Assess for malaria.
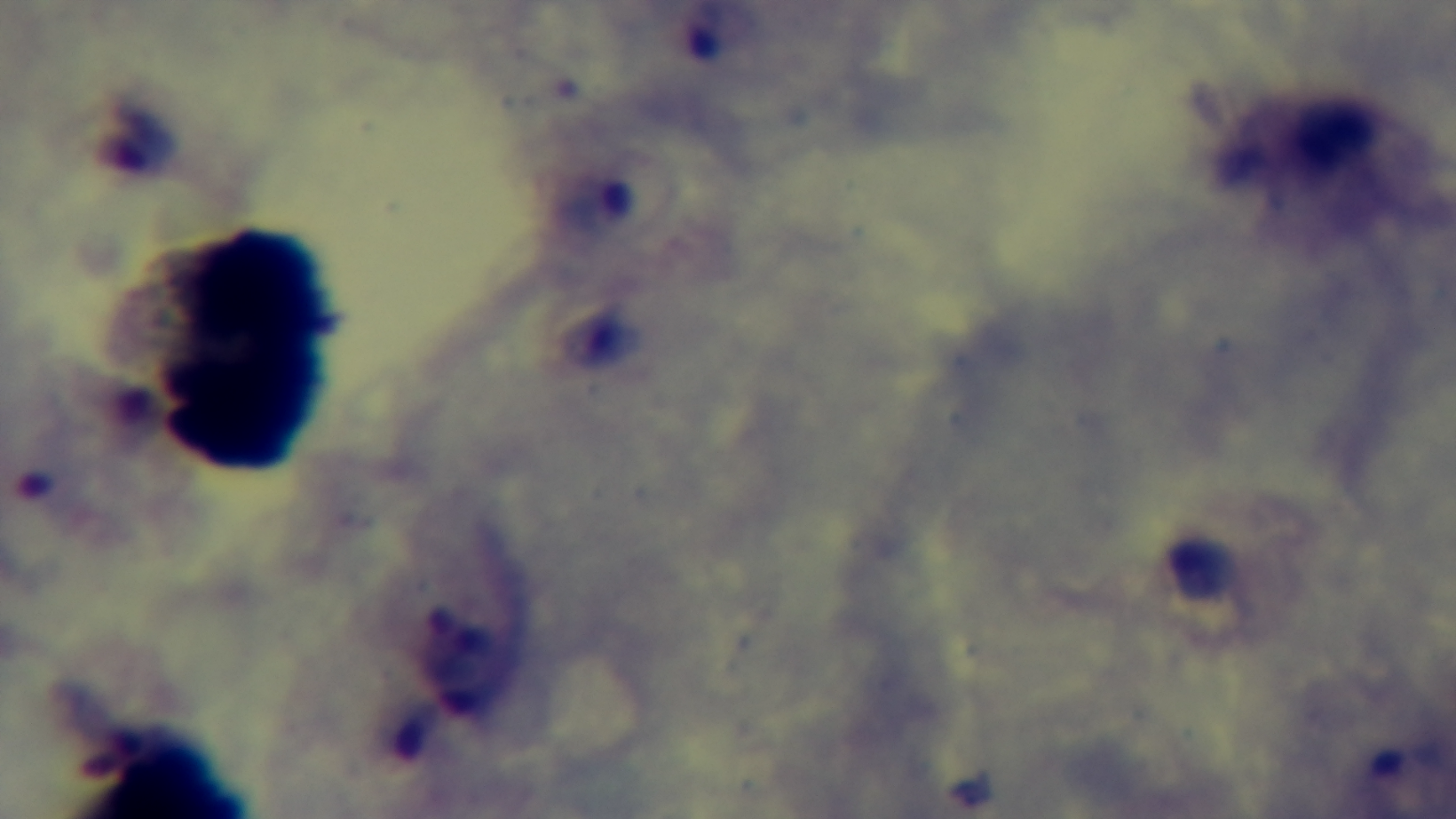
Infected.

Summary:
  - Field of view: one from the slide
  - Stain: Giemsa
  - Capture: mounted 4K digital camera
  - Objective: 100x oil immersion
  - Modality: light microscopy
  - Preparation: thick